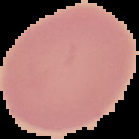

Summary:
  - Result: no Plasmodium parasites seen
  - Preparation: thin blood film
  - Image size: 139×139 pixels
  - Image type: cell region segmented out of the field of view; surrounding area masked to black